Identify the parasite.
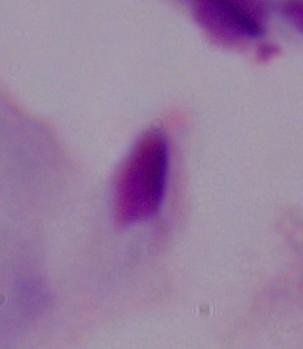
A trichomonad.

{
  "magnification": "1000x",
  "modality": "photomicrograph"
}